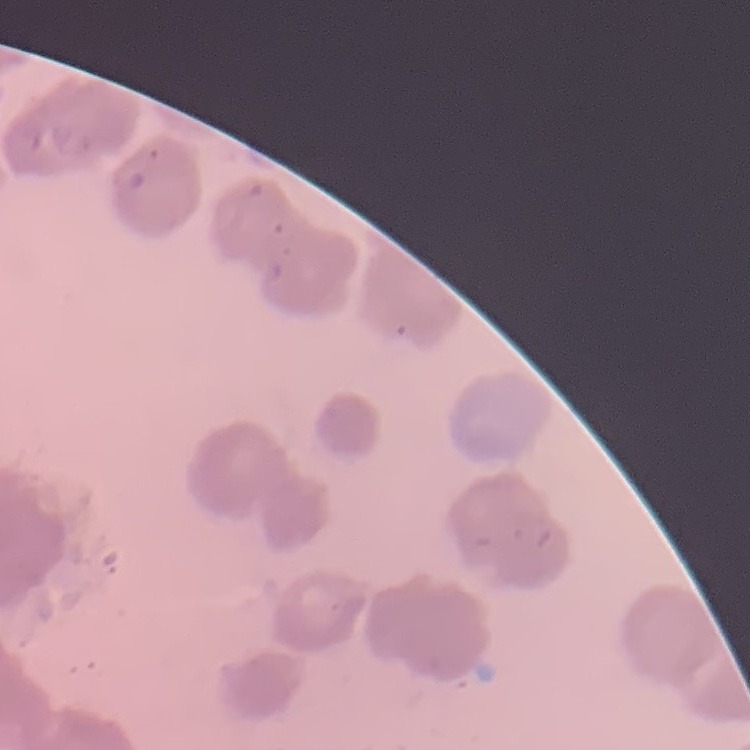
red blood cell morphology = rouleaux formation
preparation = thin blood film
stain = Field's or Giemsa
image type = square crop of a larger photomicrograph